State which parasite is depicted.
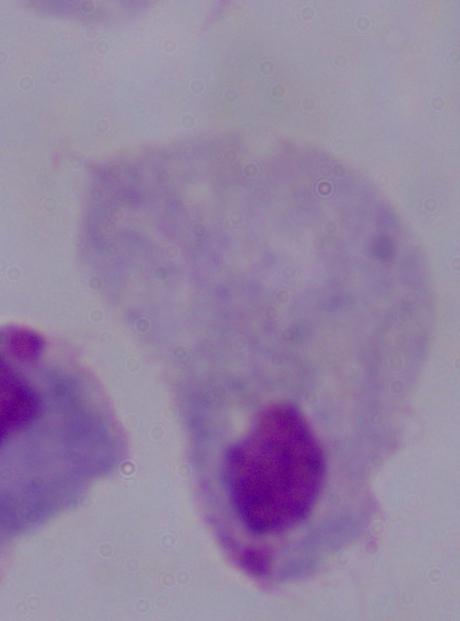

This is a trichomonad.

Summary:
  - Modality: micrograph
  - Magnification: 1000x